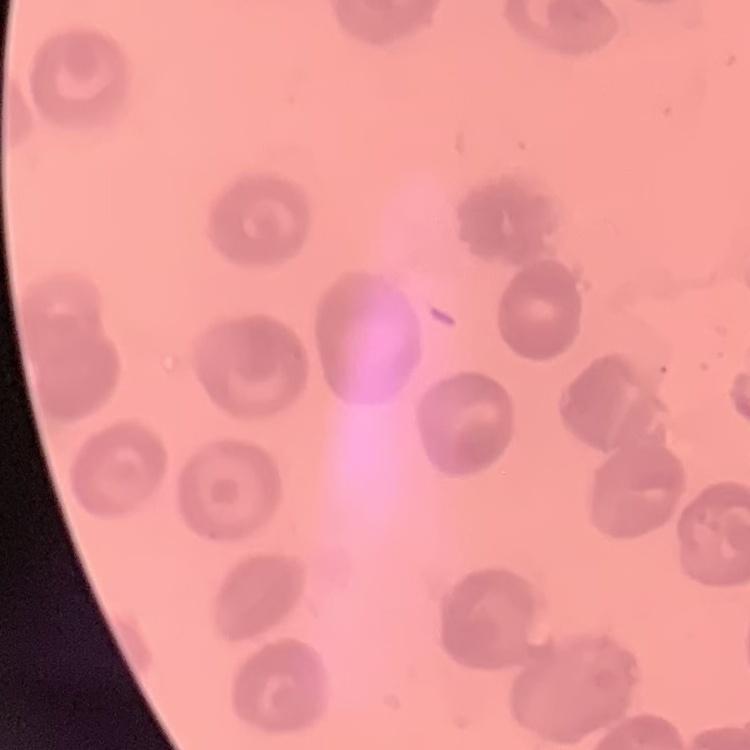
The erythrocytes exhibit no rouleaux formation. Thin blood smear. Square crop of a larger photomicrograph. Field's or Giemsa stain.